Classify this cell by malaria status.
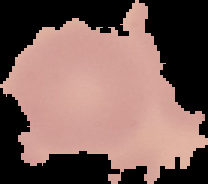

It is uninfected.

Segmented cell region on a black background. Image is 208×184 pixels. From a thin blood smear.